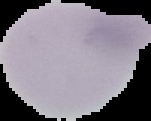

preparation = thin blood smear
image type = segmented cell region with the area outside set to black
image size = 151×121 pixels
result = negative for Plasmodium parasites